Point out leukocytes.
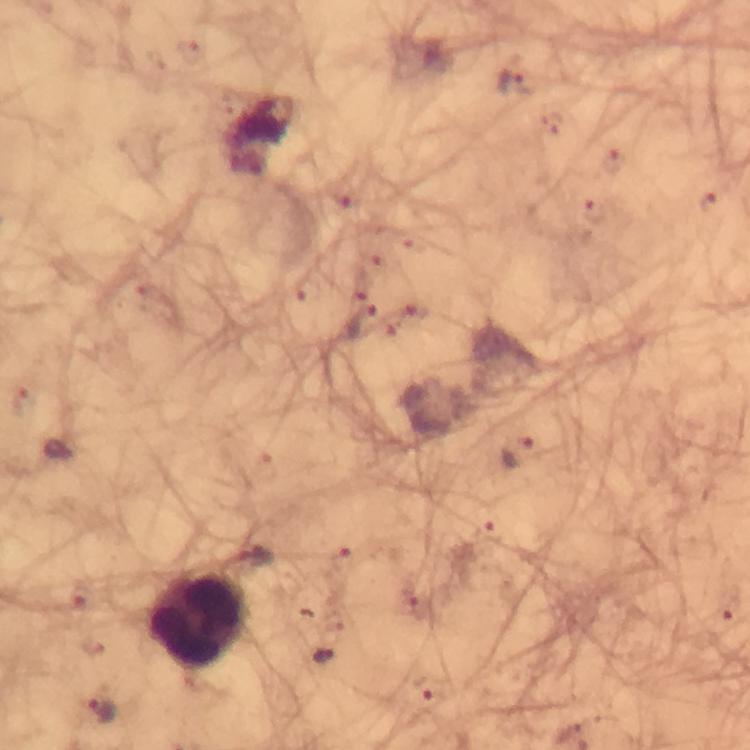
Approximate object centers, in pixels from the top-left corner.
Leukocytes: (x=200, y=620).

Malaria parasite locations: (x=512, y=82), (x=614, y=160), (x=709, y=201), (x=595, y=213), (x=360, y=321), (x=518, y=453), (x=486, y=533), (x=341, y=559), (x=322, y=656), (x=429, y=690), (x=101, y=710). Immersion oil was used. Smartphone photograph taken through a microscope. At 100x magnification. Cropped region of a single field of view. Thick blood film. Image is 750×750 pixels. From a diagnostic examination for malaria. Giemsa-stained preparation.